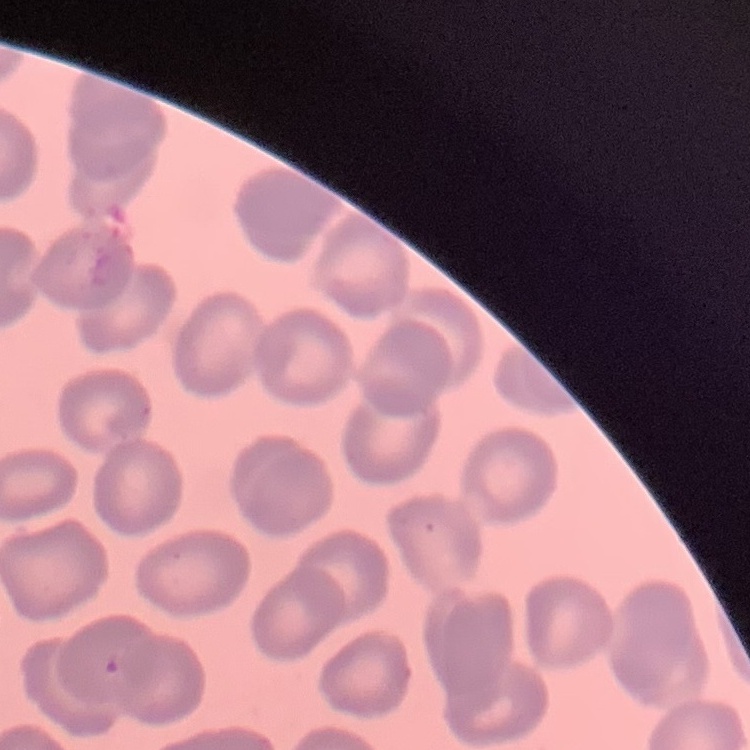

red blood cell morphology = no rouleaux formation
image type = square crop of a larger photomicrograph
preparation = thin blood smear
stain = Field's or Giemsa